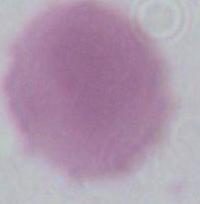

{
  "modality": "micrograph",
  "magnification": "1000x",
  "identification": "erythrocyte"
}